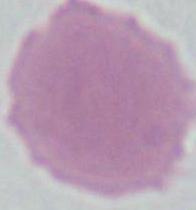 Photomicrograph. An erythrocyte is seen. Captured at 1000x magnification.